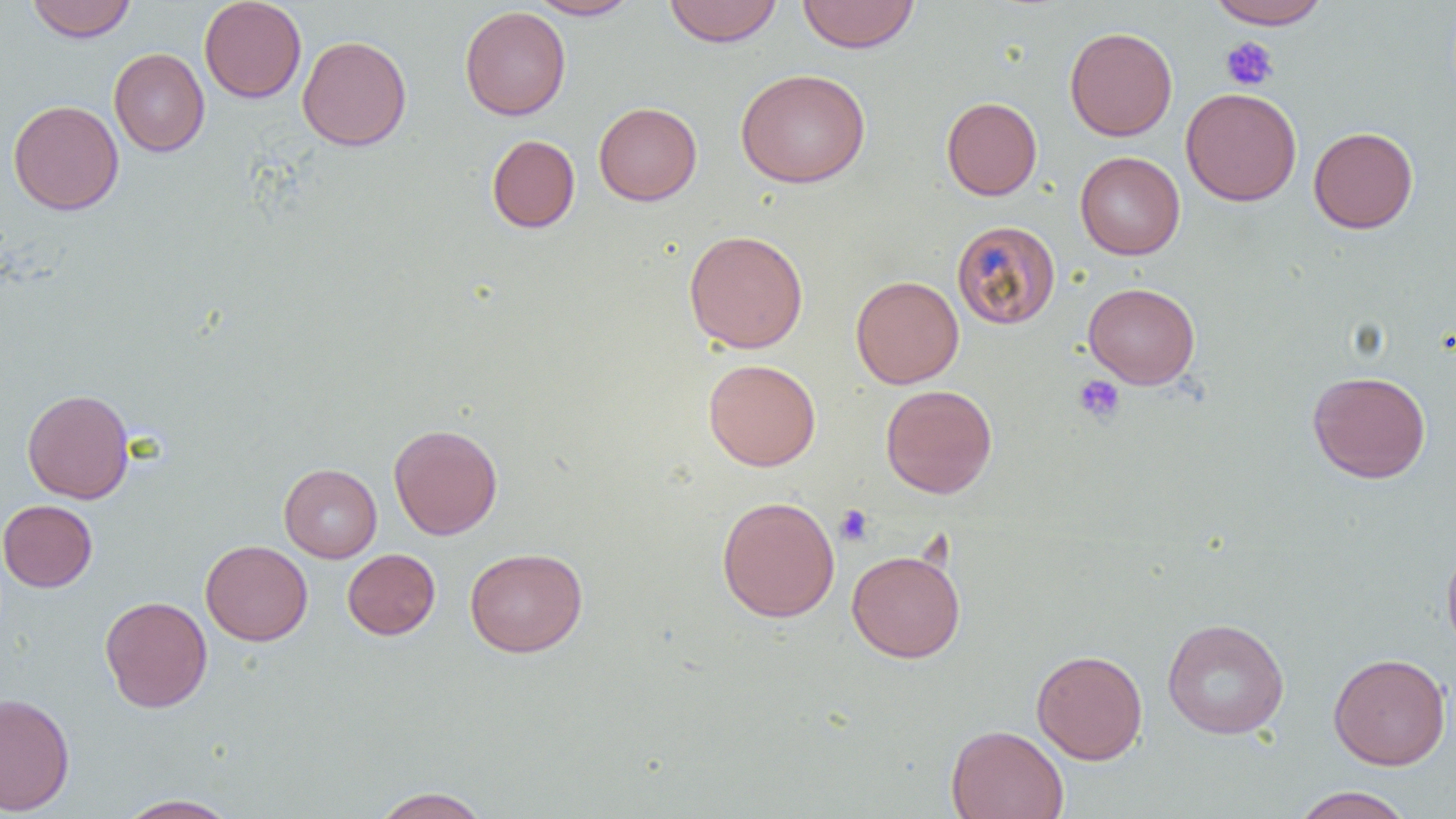

Summary:
  - Coordinate format: approximate bounding boxes as (x1,y1)-(x2,y2) corner pairs in pixels
  - Platelet locations: (1220,37)-(1278,91), (1073,374)-(1126,424), (835,504)-(873,546)
  - Uninfected red blood cell locations: (26,0)-(137,42), (199,0)-(307,103), (527,0)-(642,20), (663,0)-(782,47), (797,0)-(920,53), (1207,0)-(1331,29), (459,5)-(571,120), (1064,26)-(1177,141), (297,34)-(412,151), (109,48)-(210,157), (736,68)-(871,188), (1180,87)-(1302,206), (941,96)-(1042,200), (8,99)-(124,215), (594,102)-(702,206), (1308,126)-(1419,233), (486,134)-(580,233), (1075,151)-(1185,260), (951,220)-(1060,329), (683,229)-(809,354), (850,275)-(964,389), (1083,282)-(1201,389), (703,358)-(821,471), (1307,370)-(1431,483), (881,384)-(997,498), (21,388)-(135,504), (389,423)-(503,540), (279,463)-(382,562), (716,495)-(840,622), (0,500)-(98,592), (1441,538)-(1456,656), (200,540)-(313,646), (464,547)-(587,657), (342,548)-(440,640), (846,549)-(966,663), (99,595)-(213,713), (1162,617)-(1290,739), (1031,649)-(1148,764), (1328,652)-(1451,770), (0,692)-(75,815), (946,724)-(1069,819), (1291,786)-(1415,819), (371,787)-(492,818), (115,794)-(242,818)
  - Slide-level diagnosis: no evidence of blood parasites
  - Modality: optical microscopy
  - Field of view: single
  - Magnification: 1000x
  - Image size: 1456×819 pixels
  - Preparation: thin blood film